Assess the morphology of the red blood cells.
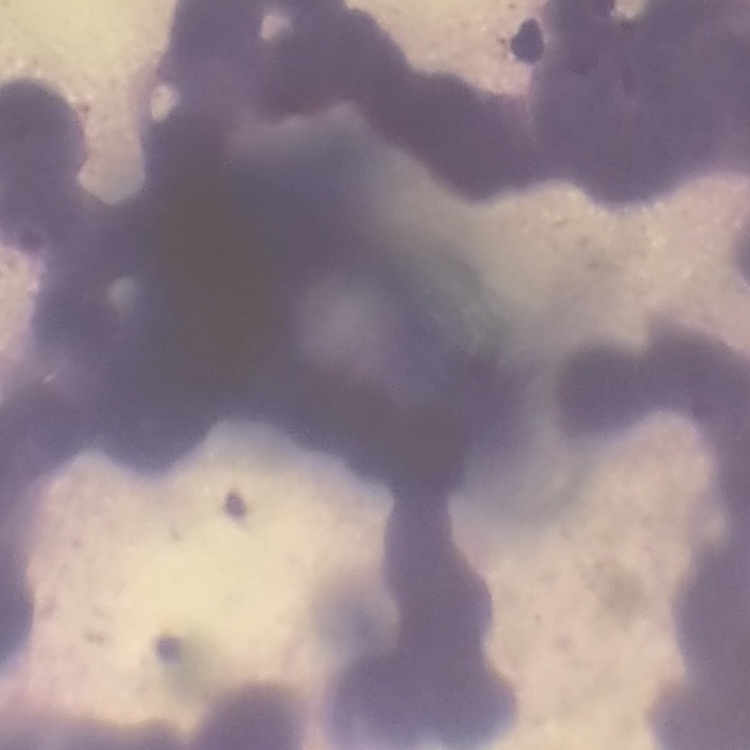

Rouleaux formation.

Stained with either Field's or Giemsa. One tile cut from a larger photomicrograph. Thin blood smear.